Report the malaria status of this cell.
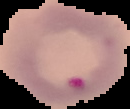

It is parasitized.

Cell region segmented out of the field of view; the surrounding area is masked to black. Image is 130×109 pixels. From a thin blood smear.